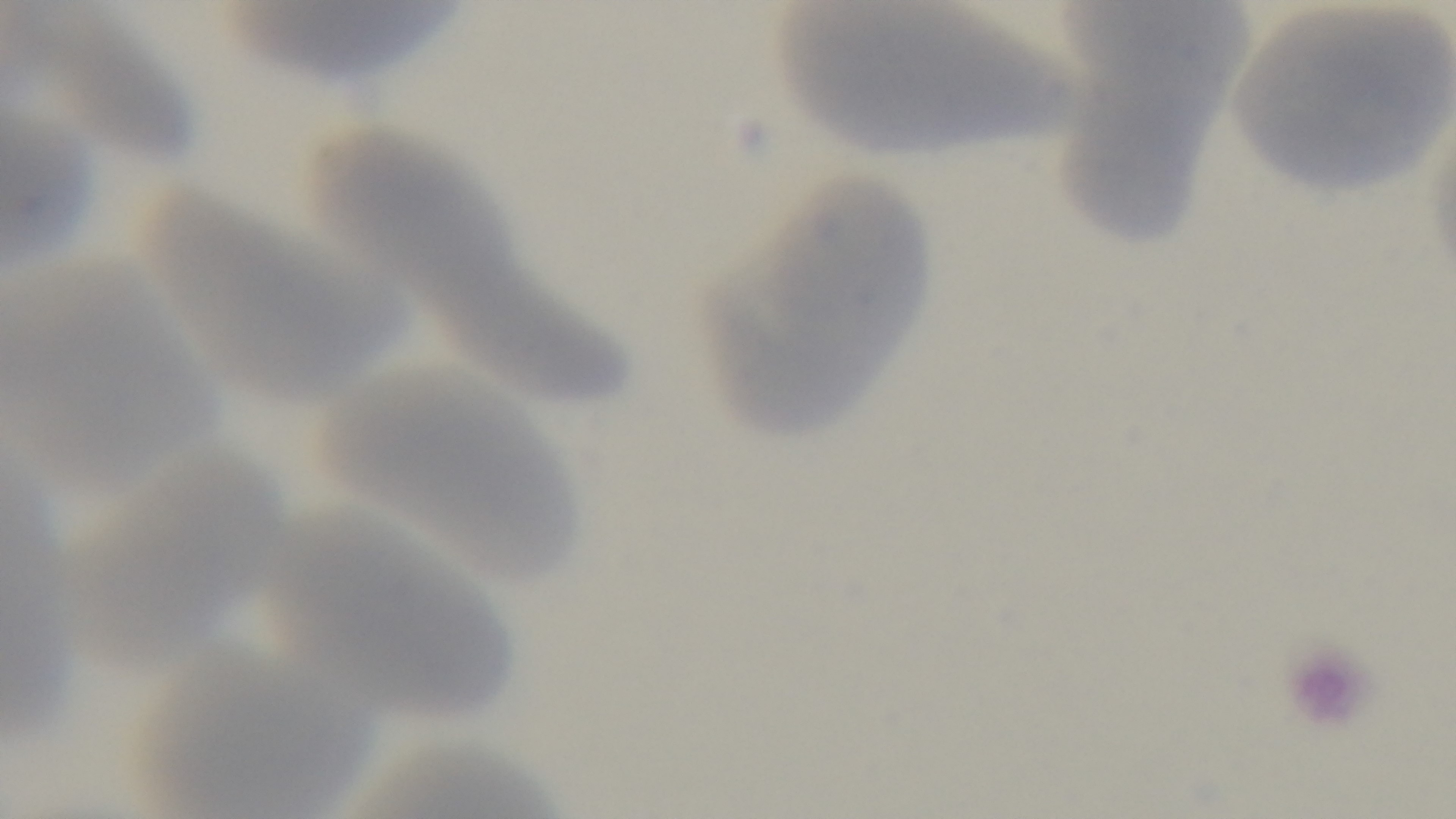 Giemsa stain. One field from the slide. Oil-immersion objective, 100x. Mounted 4K digital camera. Preparation: thin smear. Light microscopy. Malaria status: uninfected.